Identify the blood parasite species.
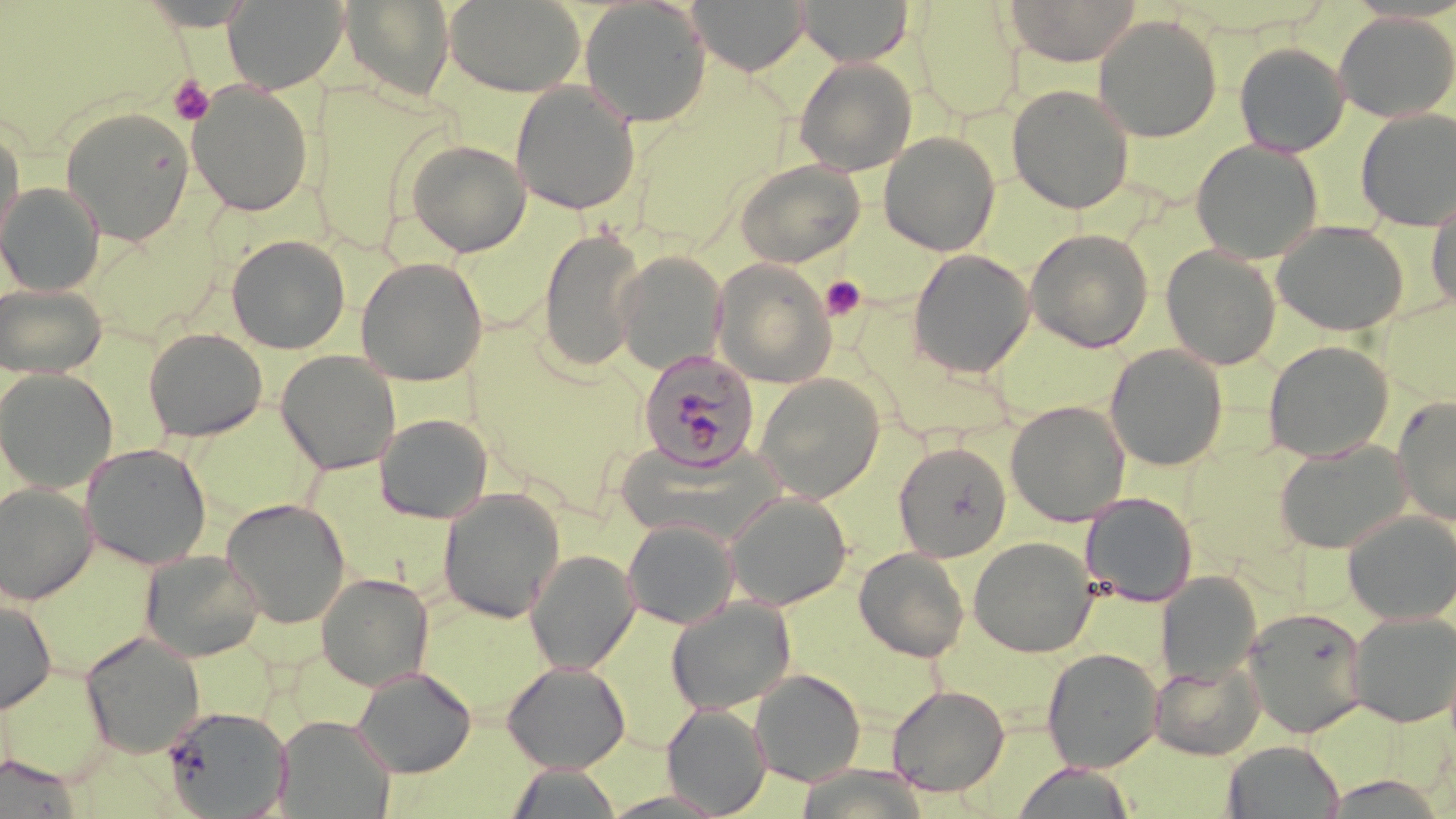

Plasmodium malariae.

Approximate bounding boxes as (x1, y1, x2, y2) in pixels. Platelet locations: (168, 76, 215, 125), (820, 276, 866, 321). Plasmodium malariae-infected red blood cell locations: (637, 350, 760, 473). Uninfected red blood cell locations: (222, 0, 348, 93), (341, 0, 455, 102), (579, 0, 712, 127), (688, 0, 810, 76), (796, 0, 913, 67), (1004, 0, 1141, 66), (134, 1, 260, 31), (444, 1, 585, 97), (913, 2, 1024, 122), (1333, 11, 1455, 122), (1093, 14, 1222, 142), (1233, 43, 1349, 157), (794, 58, 917, 176), (510, 81, 641, 216), (188, 83, 313, 216), (1007, 84, 1135, 214), (60, 107, 195, 246), (1355, 108, 1456, 231), (0, 127, 25, 264), (878, 131, 1000, 255), (405, 139, 531, 256), (1190, 140, 1323, 264), (735, 160, 864, 268), (0, 182, 104, 296), (1426, 193, 1456, 313), (1272, 220, 1410, 335), (537, 227, 646, 371), (1025, 227, 1153, 352), (226, 235, 350, 354), (1161, 245, 1281, 369), (907, 249, 1035, 378), (615, 250, 727, 374), (355, 257, 488, 386), (712, 259, 836, 387), (0, 283, 108, 379), (143, 328, 267, 442), (1263, 340, 1394, 462), (1105, 344, 1228, 471), (276, 351, 401, 475), (0, 368, 119, 493), (754, 373, 885, 502), (1392, 395, 1456, 525), (1005, 401, 1130, 526), (374, 413, 492, 523), (609, 439, 779, 541), (1274, 439, 1413, 553), (894, 442, 1011, 562), (80, 443, 212, 570), (0, 482, 97, 604), (438, 487, 565, 624), (724, 490, 852, 610), (1080, 492, 1198, 607), (221, 498, 351, 629), (1342, 510, 1456, 624), (622, 517, 740, 630), (968, 537, 1098, 658), (854, 546, 970, 661), (138, 549, 266, 662), (525, 550, 639, 674), (316, 572, 435, 691), (1157, 572, 1261, 686), (666, 597, 796, 716), (0, 598, 56, 714), (1243, 606, 1369, 737), (1347, 611, 1456, 727), (80, 632, 206, 759), (1041, 647, 1162, 773), (1150, 657, 1265, 760), (502, 660, 631, 773), (351, 665, 476, 778), (750, 668, 865, 786), (886, 684, 1010, 797), (662, 704, 770, 817), (161, 705, 292, 818), (276, 715, 394, 817), (1222, 740, 1345, 819), (0, 755, 82, 818), (505, 763, 623, 819), (1011, 763, 1137, 819). May-Grünwald-Giemsa-stained preparation. Thin blood film. Captured at 1000x magnification. Image is 1456×819 pixels. Single field of view. Light microscopy.